Describe the morphology of the erythrocytes.
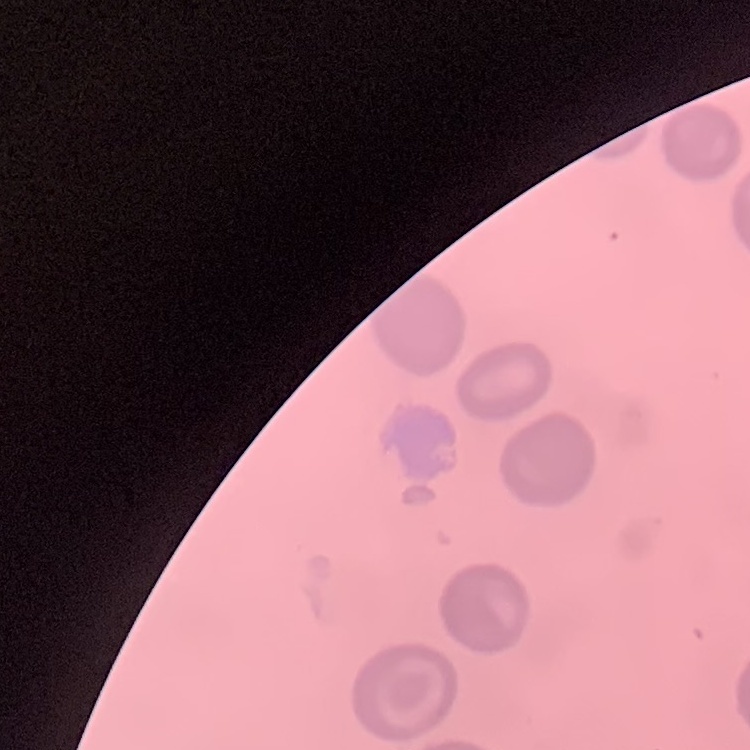
No rouleaux formation.

Field's or Giemsa stain. Thin blood film. Square crop of a larger photomicrograph.